Evaluate for Plasmodium parasites.
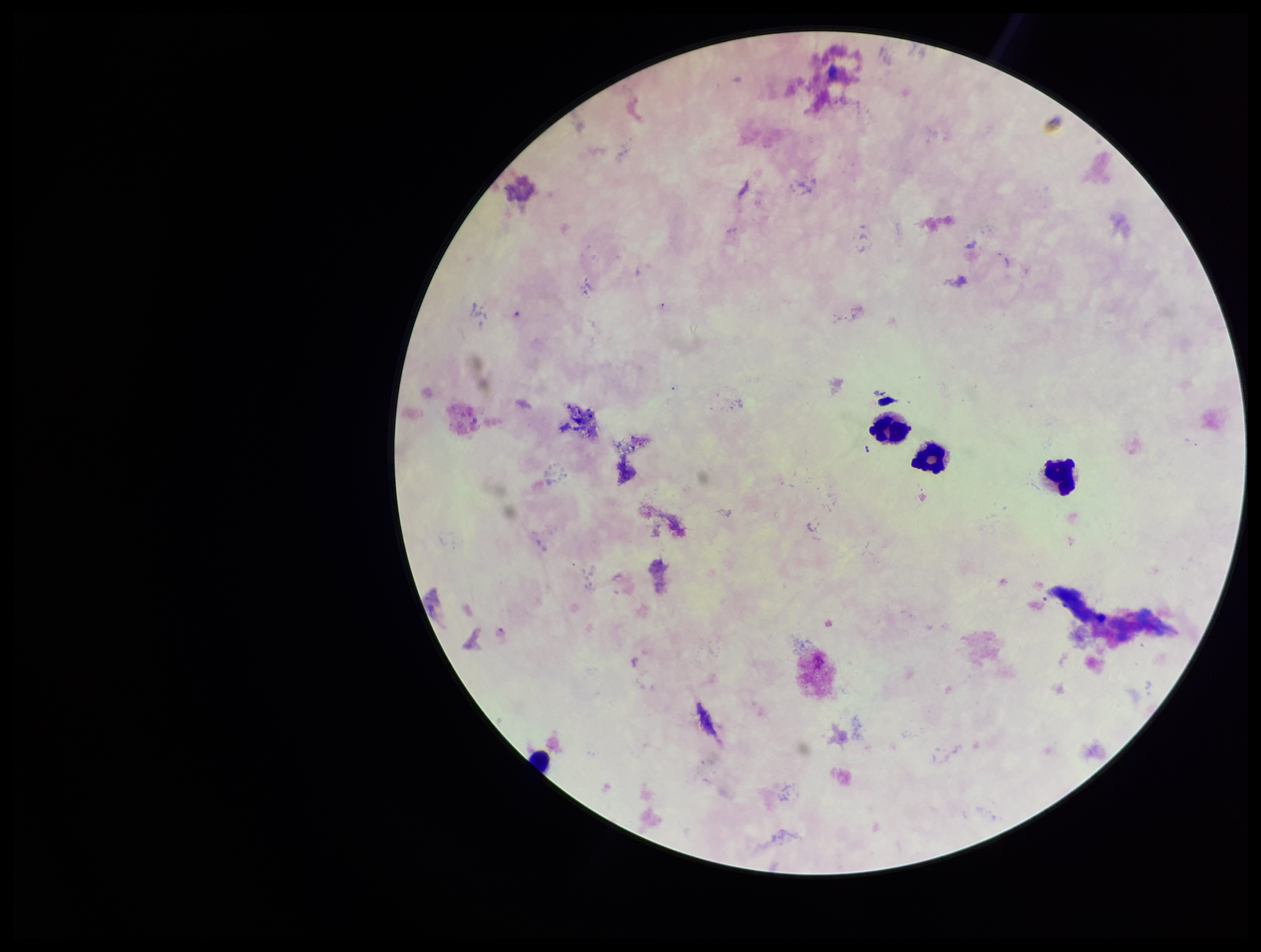
Identified.

Preparation: thick smear. One field from this slide. Parasite count: 1. Species reported for this patient: Plasmodium falciparum. Leukocyte count: 4. Stained with Giemsa. Image is 1261×952 pixels. Photographed through the microscope eyepiece with a smartphone camera. Patient malaria status: positive.